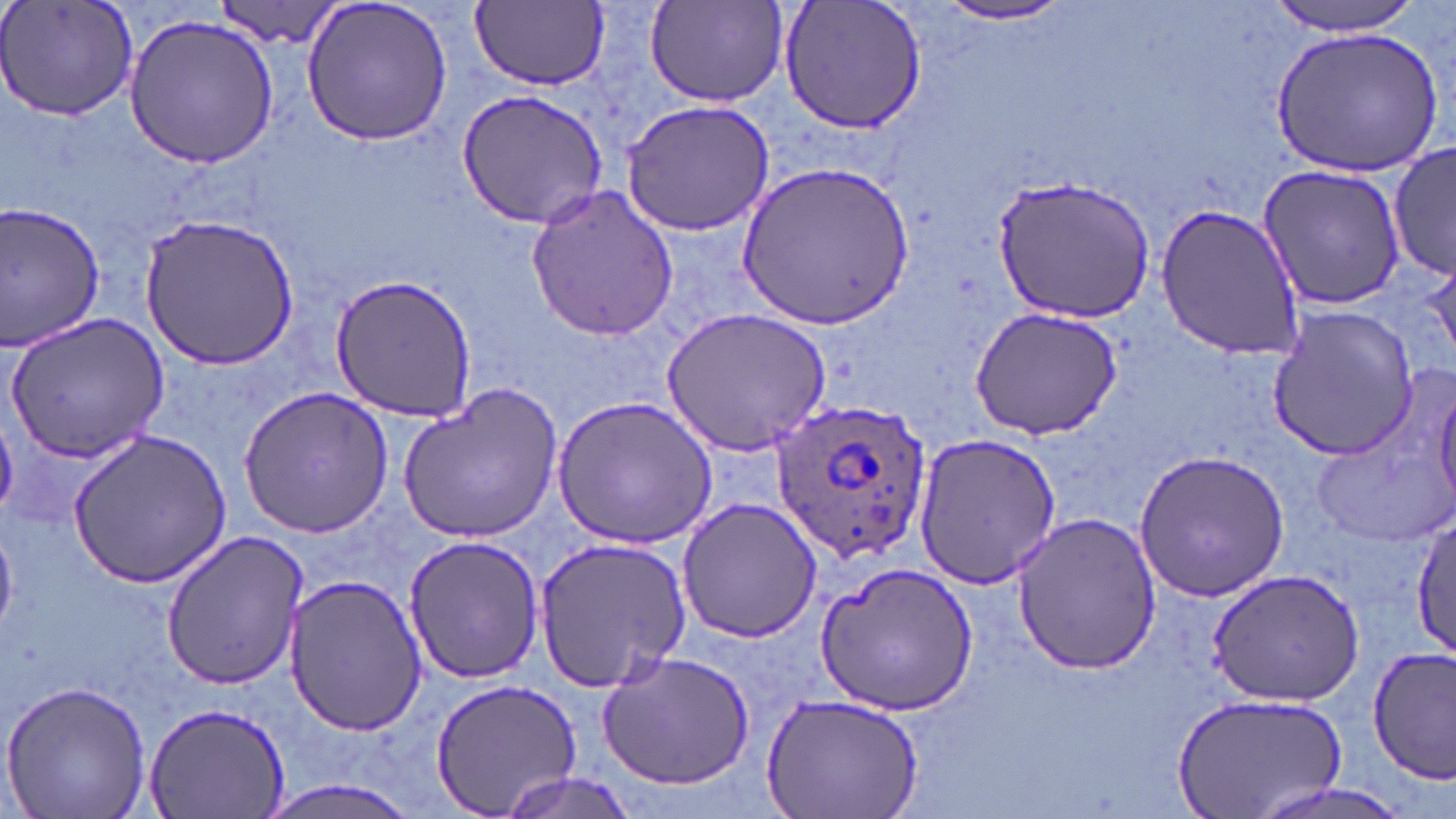
Approximate bounding boxes as (x1,y1)-(x2,y2) corner pairs in pixels. Uninfected red blood cell locations: (0,0)-(142,123), (302,0)-(454,146), (471,0)-(609,89), (779,0)-(927,135), (1264,0)-(1428,35), (646,2)-(789,108), (934,2)-(1076,27), (208,3)-(353,49), (123,12)-(279,170), (1272,25)-(1442,176), (455,89)-(610,229), (621,98)-(776,236), (1389,143)-(1453,284), (741,161)-(916,330), (1256,164)-(1407,311), (995,176)-(1156,320), (525,184)-(679,341), (0,201)-(106,355), (1156,202)-(1304,359), (141,213)-(300,371), (329,274)-(478,420), (968,306)-(1124,440), (662,307)-(830,455), (1267,307)-(1421,461), (6,313)-(169,459), (397,381)-(563,544), (1435,381)-(1456,514), (240,386)-(394,536), (554,396)-(716,548), (67,428)-(235,589), (914,431)-(1065,589), (1134,448)-(1290,601), (677,496)-(821,643), (1010,512)-(1162,676), (1412,513)-(1456,658), (159,530)-(307,691), (404,535)-(545,684), (533,535)-(692,694), (814,559)-(976,714), (1208,568)-(1366,707), (284,576)-(429,736), (1369,646)-(1456,781), (596,650)-(756,789), (427,676)-(583,819), (1,679)-(154,819), (761,692)-(924,818), (1171,692)-(1348,818), (141,701)-(290,819), (494,771)-(637,819), (258,776)-(423,819), (1247,778)-(1416,819). Plasmodium ovale-infected red blood cell locations: (770,393)-(935,570). Slide-level diagnosis: Plasmodium ovale. Single field of view. Light microscopy. Thin blood smear. Image is 1456×819 pixels. May-Grünwald-Giemsa stain. Captured at 1000x magnification.